Outline each blood parasite and name the species.
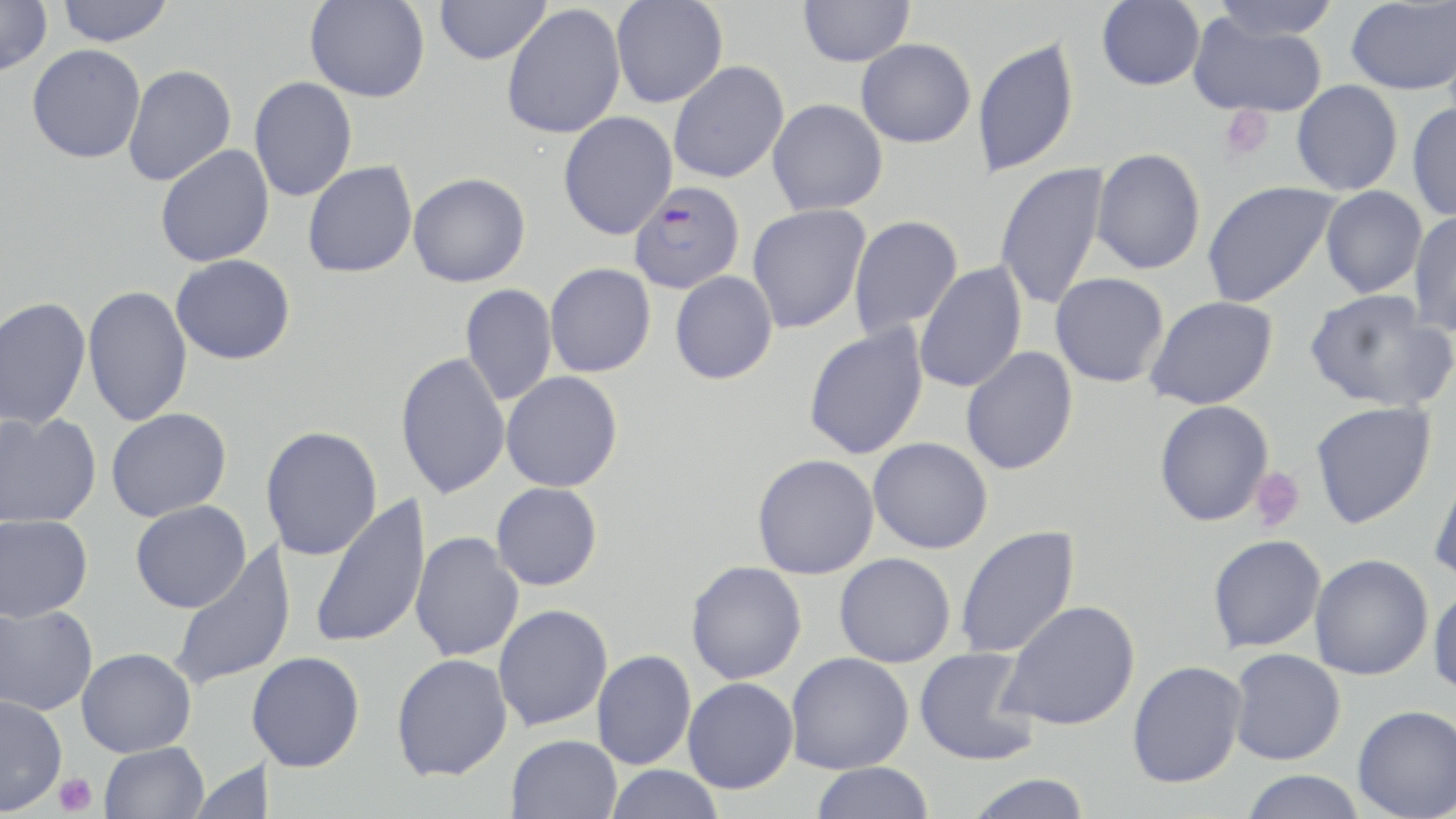
Approximate bounding boxes as (x1,y1)-(x2,y2) corner pairs in pixels.
Plasmodium falciparum-infected red blood cells: (629,181)-(745,294).
No Plasmodium ovale, Plasmodium malariae, Plasmodium vivax, Babesia divergens, or Trypanosoma brucei observed.

Uninfected red blood cell locations: (0,0)-(52,77), (55,0)-(173,46), (305,0)-(430,102), (433,0)-(551,65), (798,0)-(915,67), (1096,0)-(1205,90), (1209,0)-(1341,41), (1346,0)-(1456,95), (610,1)-(727,109), (501,4)-(626,139), (1188,13)-(1328,118), (972,36)-(1079,178), (856,39)-(976,148), (26,44)-(146,163), (668,61)-(789,183), (122,64)-(236,187), (248,76)-(357,202), (1291,80)-(1403,196), (767,98)-(888,216), (1407,102)-(1456,222), (558,111)-(678,240), (154,144)-(275,267), (1091,148)-(1206,275), (302,160)-(418,278), (995,162)-(1109,312), (408,172)-(531,287), (1202,180)-(1339,308), (1320,186)-(1427,299), (747,204)-(870,334), (1409,209)-(1456,336), (848,215)-(963,342), (170,254)-(296,365), (914,261)-(1027,394), (544,262)-(656,377), (670,271)-(778,384), (1050,272)-(1169,387), (459,283)-(558,407), (83,284)-(193,427), (1304,288)-(1455,412), (1144,295)-(1279,410), (0,296)-(91,430), (803,324)-(929,460), (960,346)-(1078,475), (395,352)-(510,499), (501,371)-(623,492), (1154,400)-(1274,526), (1310,401)-(1436,529), (106,408)-(232,522), (0,412)-(101,528), (260,425)-(383,561), (868,437)-(993,554), (751,454)-(879,579), (1428,463)-(1456,584), (491,482)-(603,591), (309,494)-(432,650), (130,500)-(251,613), (0,514)-(94,622), (954,525)-(1080,659), (410,532)-(524,663), (1207,534)-(1326,652), (166,539)-(297,693), (834,552)-(956,667), (1309,554)-(1433,679), (685,561)-(807,684), (1428,586)-(1456,698), (998,600)-(1141,731), (0,603)-(99,715), (493,603)-(613,731), (77,647)-(196,757), (914,647)-(1040,767), (1227,648)-(1345,765), (592,650)-(696,770), (248,651)-(365,772), (785,651)-(914,774), (391,653)-(512,781), (1127,660)-(1247,788), (683,677)-(798,794), (0,694)-(67,816), (1352,704)-(1456,818), (506,734)-(622,819), (99,742)-(210,819), (187,759)-(269,818), (810,762)-(934,819), (604,765)-(726,818), (1240,770)-(1366,819), (963,774)-(1093,819). Platelet locations: (1219,105)-(1275,162), (1248,467)-(1306,532), (54,772)-(97,817). Slide-level diagnosis: Plasmodium falciparum. Captured at 1000x magnification. Image is 1456×819 pixels. Thin blood film. May-Grünwald-Giemsa stain. Optical microscopy. Single field of view.